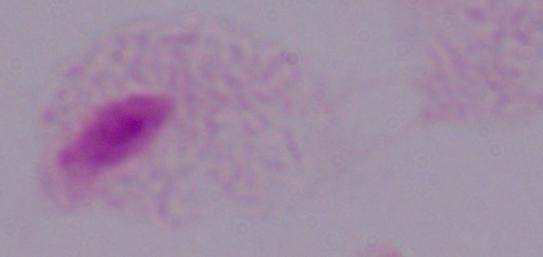
A trichomonad is seen. Captured at 1000x magnification. Micrograph.